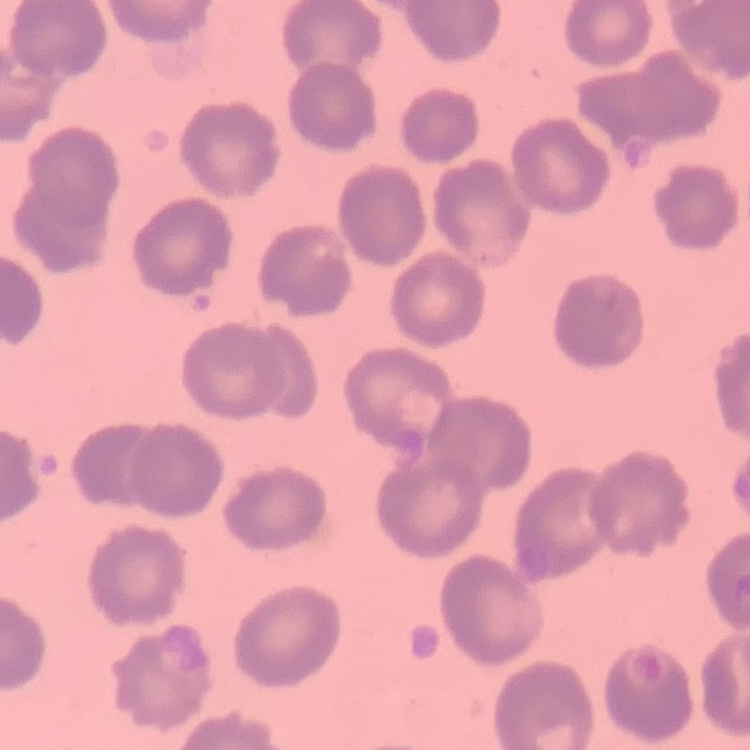

red blood cell morphology = no rouleaux formation
preparation = thin peripheral smear
stain = Field's or Giemsa
image type = one tile cut from a larger photomicrograph